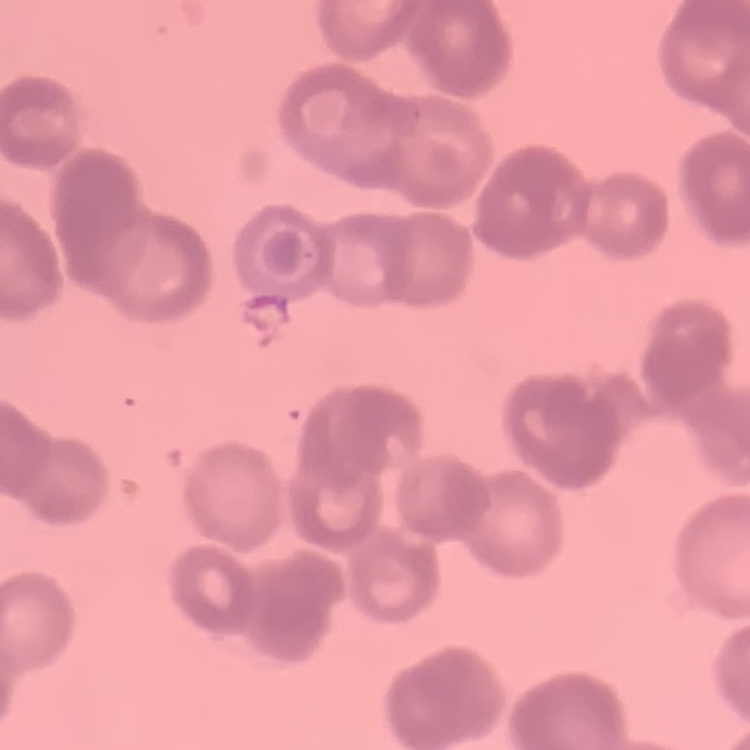 The red blood cells exhibit rouleaux formation. Square crop of a larger photomicrograph. Thin peripheral smear. Stained with either Field's or Giemsa.